Locate and identify every blood parasite.
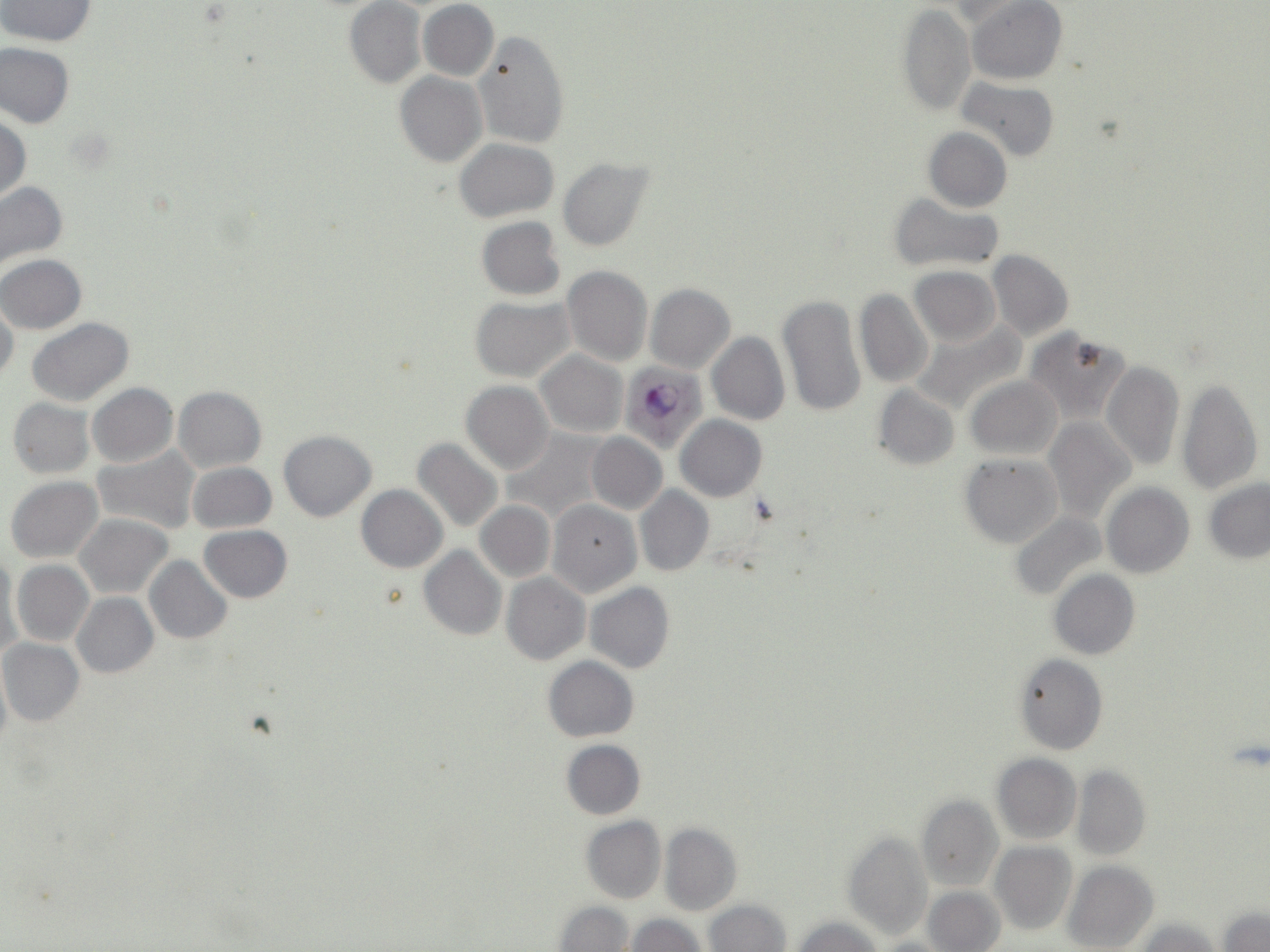
Approximate bounding boxes as (x1, y1, x2, y2) in pixels.
Plasmodium falciparum-infected red blood cells: (620, 362, 709, 450).
No Plasmodium ovale, Plasmodium malariae, Plasmodium vivax, Babesia divergens, or Trypanosoma brucei observed.

Uninfected red blood cell locations: (0, 0, 98, 46), (968, 1, 1067, 85), (344, 2, 425, 88), (417, 2, 499, 81), (897, 3, 975, 116), (939, 3, 1021, 27), (473, 30, 570, 149), (1, 42, 75, 128), (395, 72, 487, 167), (955, 77, 1059, 162), (0, 114, 30, 204), (922, 127, 1012, 212), (454, 138, 559, 222), (557, 157, 654, 252), (0, 181, 69, 274), (888, 193, 1005, 273), (476, 216, 565, 300), (988, 250, 1074, 340), (1, 254, 86, 333), (562, 265, 653, 367), (909, 266, 1001, 347), (645, 284, 734, 373), (854, 288, 934, 388), (777, 294, 864, 418), (471, 297, 574, 382), (0, 302, 19, 385), (27, 318, 136, 406), (910, 319, 1026, 416), (1025, 327, 1132, 426), (707, 331, 790, 425), (536, 350, 627, 437), (1100, 360, 1184, 472), (965, 375, 1062, 460), (1175, 378, 1261, 494), (461, 381, 553, 475), (88, 383, 178, 466), (872, 385, 959, 470), (174, 386, 266, 472), (8, 397, 96, 480), (676, 415, 767, 502), (1045, 416, 1134, 522), (278, 430, 376, 521), (500, 430, 612, 523), (586, 433, 666, 514), (412, 437, 503, 535), (92, 445, 201, 535), (959, 454, 1061, 547), (187, 462, 277, 533), (6, 476, 102, 562), (1203, 476, 1270, 565), (1103, 484, 1194, 578), (356, 485, 447, 572), (636, 486, 714, 575), (548, 500, 641, 597), (475, 501, 555, 582), (1010, 512, 1107, 602), (75, 514, 172, 598), (199, 525, 293, 603), (419, 545, 506, 640), (1, 554, 23, 665), (144, 555, 233, 644), (12, 560, 94, 646), (1049, 570, 1139, 660), (502, 573, 589, 665), (585, 582, 675, 674), (72, 593, 158, 678), (0, 639, 84, 725), (1013, 654, 1107, 755), (543, 656, 638, 741), (0, 661, 11, 761), (562, 740, 645, 820), (992, 753, 1082, 843), (1070, 764, 1151, 860), (917, 796, 1002, 891), (581, 816, 665, 904), (659, 823, 742, 915), (841, 830, 933, 941), (989, 842, 1076, 934), (1062, 861, 1160, 952), (924, 885, 1005, 952), (704, 900, 791, 951), (555, 901, 635, 951), (1216, 906, 1269, 951), (625, 915, 706, 951), (792, 916, 882, 952), (1133, 918, 1219, 951). Platelet locations: (1226, 738, 1270, 771). Slide-level diagnosis: Plasmodium falciparum. May-Grünwald-Giemsa stain. Single field of view. Thin blood smear. Optical microscopy. Image is 1270×952 pixels. Captured at 1000x magnification.